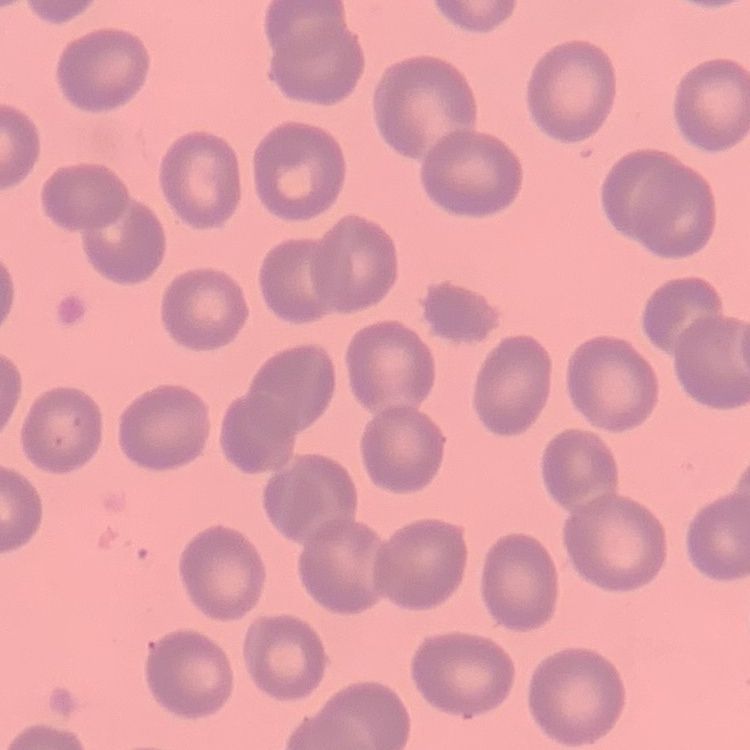 The erythrocytes show no rouleaux formation. Square crop of a larger photomicrograph. Stained with either Field's or Giemsa. Thin blood film.